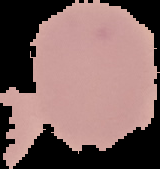

preparation = thin blood film
malaria status = uninfected
image type = cell region segmented out of the field of view; surrounding area masked to black
image size = 160×169 pixels